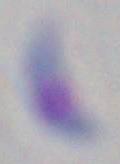

1000x magnification. Toxoplasma gondii is seen. Micrograph.